Classify this cell by malaria status.
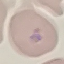

It is parasitized.

Thin blood film. Giemsa stain. Acquired by smartphone through the microscope eyepiece. Automatically extracted cell patch, resized to 64 × 64 pixels.